Assess this cell for malaria.
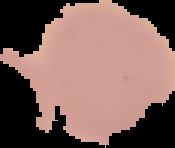

It is uninfected.

preparation: thin blood film
image_size: 175×148 pixels
image_type: segmented cell region on a black background